Give the extent of all Plasmodium falciparum-infected red blood cells.
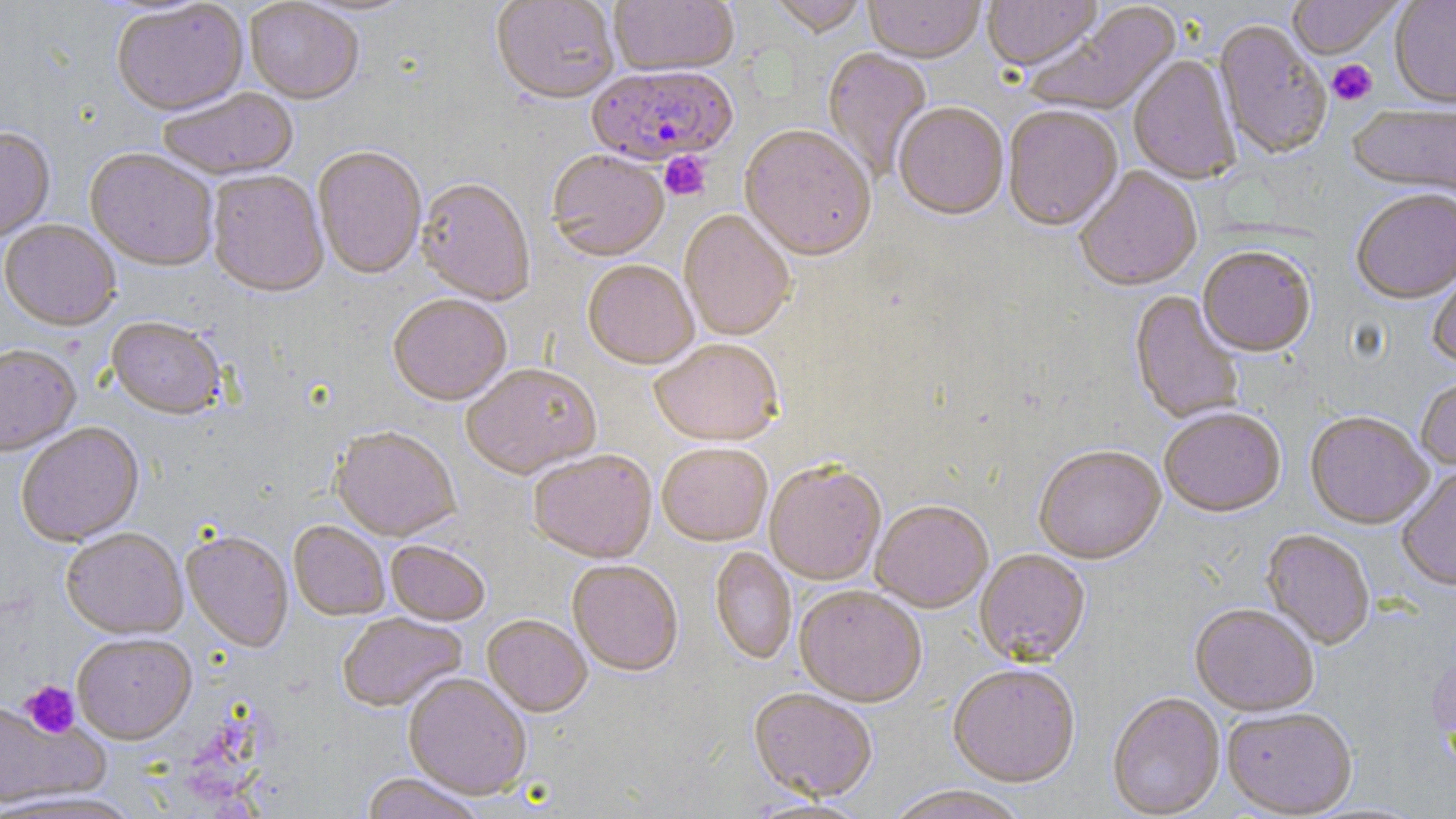

Approximate bounding boxes as [x1, y1, x2, y2] in pixels.
Plasmodium falciparum-infected red blood cells: [587, 67, 739, 170].

slide_level_diagnosis: Plasmodium falciparum
field_of_view: single
magnification: 1000x
modality: light microscopy
preparation: thin blood smear
uninfected_red_blood_cell_locations: 'approximate bounding boxes as [x1, y1, x2, y2] in pixels: [295, 0, 419, 18], [491, 0, 619, 107], [610, 0, 738, 79], [768, 0, 868, 39], [864, 0, 984, 66], [982, 0, 1103, 74], [1287, 0, 1403, 61], [1390, 0, 1456, 110], [245, 1, 363, 106], [111, 2, 249, 119], [1027, 4, 1184, 119], [1213, 21, 1332, 162], [822, 48, 933, 180], [1128, 56, 1241, 187], [158, 89, 300, 182], [894, 105, 1009, 223], [1348, 105, 1456, 198], [1003, 107, 1123, 234], [739, 127, 877, 264], [0, 128, 55, 243], [313, 148, 427, 282], [84, 150, 217, 273], [547, 152, 669, 264], [1075, 168, 1202, 294], [207, 172, 328, 300], [415, 180, 535, 308], [1351, 191, 1456, 306], [679, 210, 795, 344], [1, 221, 121, 333], [1198, 249, 1315, 359], [1427, 259, 1456, 372], [582, 262, 699, 373], [1130, 291, 1244, 426], [388, 297, 511, 409], [106, 318, 227, 421], [649, 341, 784, 449], [0, 345, 82, 458], [462, 366, 602, 482], [1416, 378, 1456, 474], [1159, 410, 1286, 520], [1305, 413, 1433, 531], [16, 423, 144, 547], [330, 428, 461, 544], [657, 445, 772, 548], [1034, 447, 1167, 565], [529, 452, 657, 564], [764, 464, 886, 587], [1397, 467, 1456, 592], [871, 503, 993, 614], [288, 521, 389, 621], [61, 528, 188, 639], [1261, 530, 1375, 651], [182, 532, 293, 653], [385, 542, 489, 628], [710, 547, 796, 666], [974, 551, 1090, 668], [567, 562, 683, 678], [794, 588, 927, 708], [1189, 606, 1320, 718], [338, 614, 467, 713], [482, 616, 592, 719], [72, 634, 197, 744], [948, 667, 1081, 788], [403, 675, 532, 801], [748, 690, 877, 803], [1107, 694, 1225, 818], [0, 700, 109, 809], [1221, 709, 1357, 818], [360, 773, 486, 819], [881, 787, 1030, 819], [0, 790, 145, 819]'
image_size: 1456×819 pixels
stain: May-Grünwald-Giemsa
platelet_locations: 'approximate bounding boxes as [x1, y1, x2, y2] in pixels: [1328, 60, 1377, 106], [660, 152, 710, 201], [20, 680, 80, 739]'